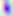

magnification = 400x
modality = photomicrograph
identification = Toxoplasma gondii